Assess the morphology of the erythrocytes.
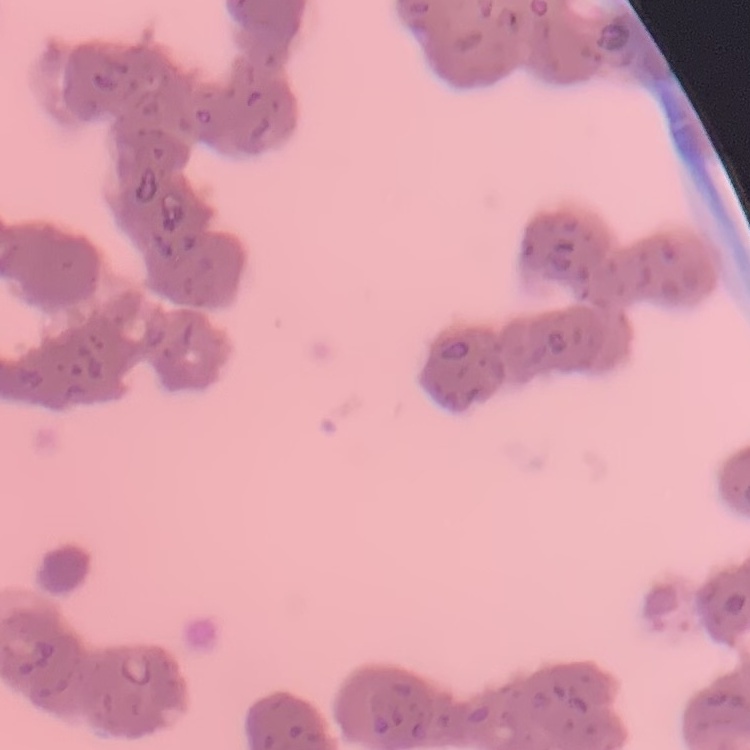
They show rouleaux formation.

Summary:
  - Preparation: thin peripheral smear
  - Image type: one tile cut from a larger photomicrograph
  - Stain: Field's or Giemsa